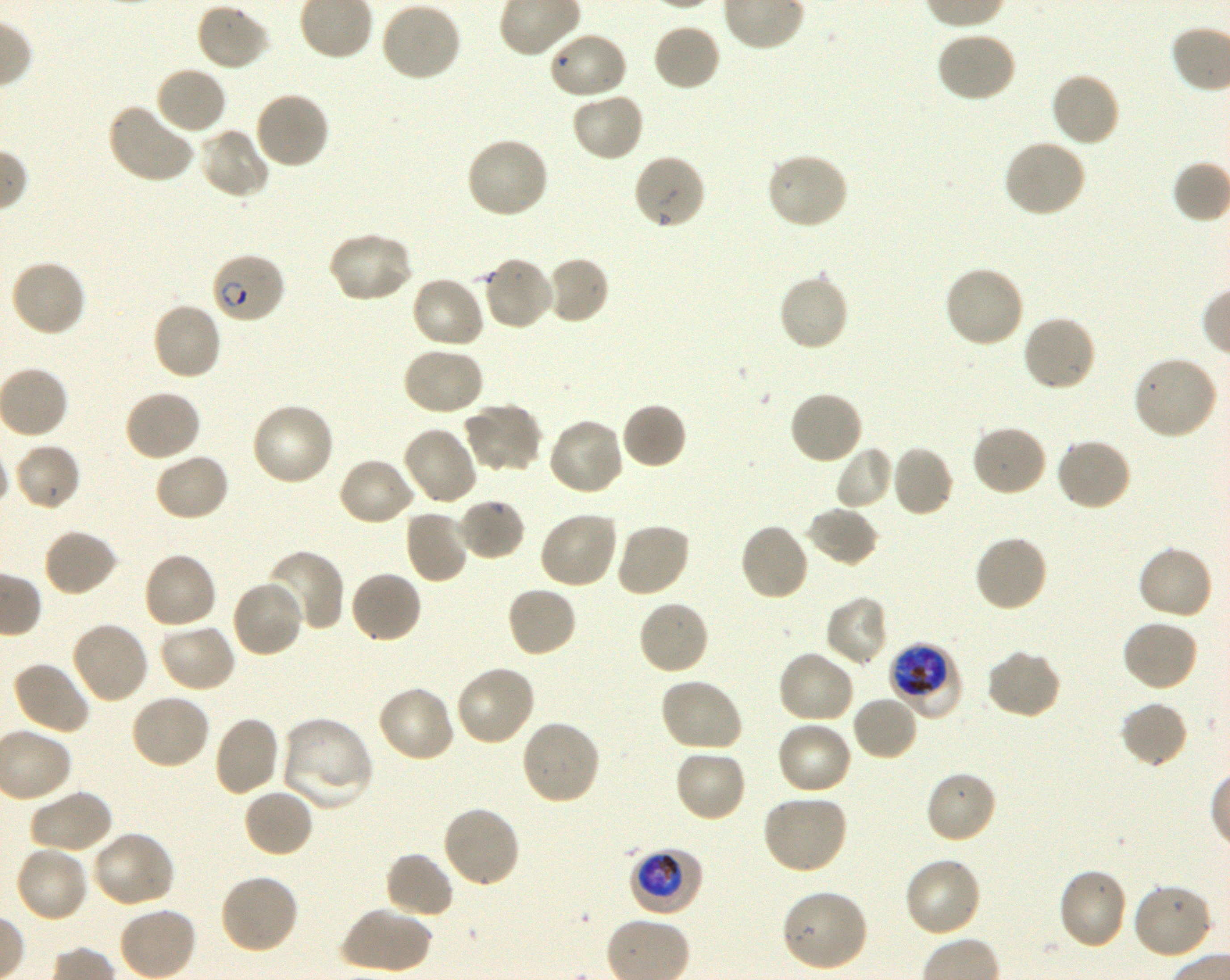
Not every red blood cell is marked. A life-cycle stage — or a range of stages, where the recorded stages span more than one — follows each staged infected red blood cell.
preparation: thin blood film
field_of_view: one from this slide
locations_of_red_blood_cells_of_indeterminate_infection_status: 'approximate bounding boxes as [x1, y1, x2, y2] in pixels: [547, 30, 628, 100]'
image_size: 1230×980 pixels
stain: Giemsa
donor_blood_group: O+
locations_of_uninfected_red_blood_cells: 'approximate bounding boxes as [x1, y1, x2, y2] in pixels: [379, 2, 462, 83], [195, 3, 272, 72], [652, 22, 721, 92], [935, 31, 1018, 104], [154, 65, 228, 136], [1049, 72, 1121, 148], [253, 90, 331, 169], [570, 91, 645, 162], [106, 101, 195, 185], [197, 126, 270, 199], [464, 136, 550, 220], [1002, 139, 1087, 219], [765, 152, 849, 230], [632, 153, 707, 230], [326, 231, 414, 304], [544, 255, 610, 325], [481, 256, 555, 332], [9, 259, 87, 339], [943, 266, 1026, 349], [777, 273, 849, 353], [410, 274, 486, 350], [151, 300, 223, 381], [1021, 314, 1098, 394], [401, 346, 485, 417], [1132, 354, 1219, 440], [122, 388, 202, 463], [788, 389, 864, 465], [249, 402, 336, 488], [463, 402, 543, 473], [620, 402, 687, 470], [546, 416, 625, 496], [971, 424, 1048, 498], [401, 425, 478, 506], [1054, 436, 1133, 512], [13, 442, 81, 511], [834, 445, 894, 511], [890, 445, 955, 518], [153, 452, 231, 523], [337, 456, 417, 528], [456, 497, 527, 562], [805, 506, 879, 568], [403, 508, 470, 585], [538, 510, 620, 590], [614, 522, 691, 598], [739, 522, 810, 602], [42, 528, 119, 598], [973, 533, 1049, 612], [1136, 545, 1214, 622], [265, 551, 346, 633], [142, 552, 219, 631], [349, 570, 423, 646], [231, 579, 304, 659], [505, 585, 578, 658], [825, 596, 889, 667], [636, 599, 710, 676], [70, 620, 151, 705], [1120, 620, 1200, 693], [157, 623, 237, 694], [985, 648, 1063, 720], [776, 650, 857, 725], [11, 660, 91, 736], [453, 664, 536, 748], [657, 677, 744, 753], [376, 684, 455, 764], [129, 693, 211, 770], [851, 695, 920, 762], [1119, 701, 1189, 769], [213, 715, 281, 797], [280, 717, 374, 813], [519, 718, 602, 807], [775, 720, 854, 797], [674, 748, 747, 823], [924, 769, 998, 845], [29, 788, 114, 855], [243, 788, 315, 858], [761, 795, 849, 875], [441, 806, 521, 889], [91, 829, 177, 908], [14, 845, 91, 925], [383, 851, 455, 921], [902, 856, 983, 938], [1057, 866, 1129, 950], [219, 873, 300, 955], [1132, 882, 1216, 962], [780, 888, 869, 973], [341, 905, 432, 975], [118, 906, 198, 980]'
locations_of_infected_red_blood_cells: 'approximate bounding boxes as [x1, y1, x2, y2] in pixels: [210, 252, 286, 325] early ring to early trophozoite; [892, 645, 964, 721] early trophozoite to late schizont; [629, 847, 704, 917] trophozoite'
objective: 100x, oil immersion, numerical aperture 1.30
culture: Plasmodium falciparum strain 3D7, shaking, in vitro